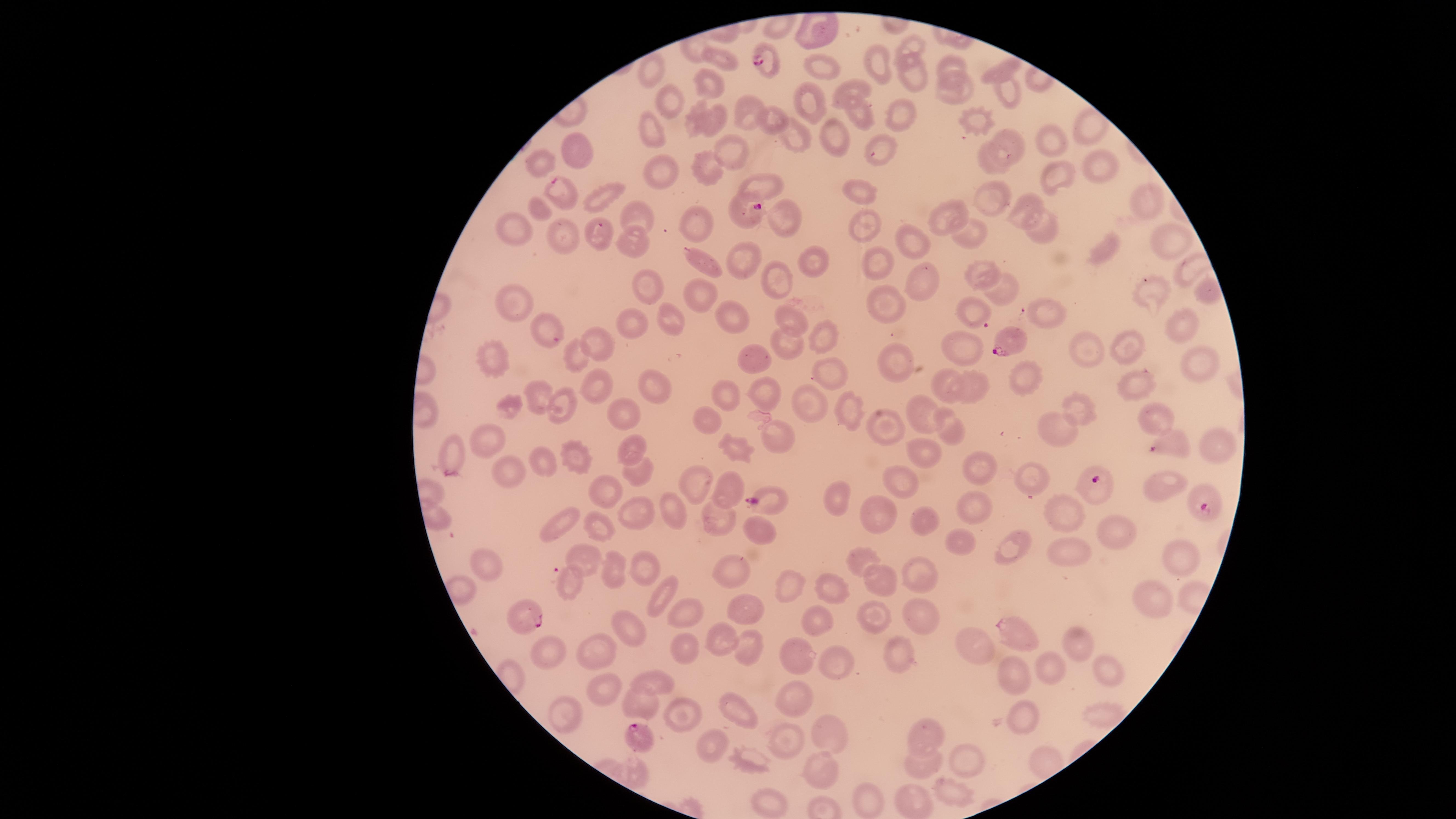
Approximate marker points as {x, y} in pixels.
Summary:
  - Parasitized RBCs: {763, 58}, {558, 190}, {748, 212}, {1008, 344}, {1163, 446}, {1096, 487}, {765, 499}, {1203, 506}, {530, 620}, {1016, 632}, {635, 736}
  - Uninfected RBCs: {912, 47}, {716, 58}, {876, 65}, {954, 66}, {818, 68}, {651, 71}, {1002, 72}, {908, 76}, {707, 83}, {951, 88}, {1004, 90}, {845, 93}, {668, 104}, {805, 107}, {903, 116}, {747, 117}, {689, 118}, {715, 118}, {771, 118}, {862, 118}, {977, 123}, {1085, 126}, {654, 134}, {833, 136}, {1014, 139}, {799, 140}, {1057, 140}, {577, 149}, {878, 151}, {730, 152}, {539, 159}, {996, 161}, {1101, 165}, {660, 171}, {711, 173}, {1047, 177}, {758, 188}, {602, 192}, {863, 193}, {991, 195}, {1139, 204}, {539, 206}, {1020, 207}, {632, 211}, {785, 219}, {952, 219}, {512, 222}, {701, 224}, {863, 227}, {1052, 228}, {598, 237}, {974, 237}, {910, 238}, {570, 241}, {1166, 241}, {633, 242}, {1103, 253}, {744, 257}, {706, 263}, {811, 263}, {987, 265}, {878, 266}, {919, 271}, {781, 280}, {999, 283}, {650, 287}, {708, 289}, {1153, 289}, {887, 296}, {512, 301}, {965, 310}, {1042, 312}, {731, 314}, {677, 317}, {788, 318}, {1185, 318}, {642, 329}, {548, 335}, {822, 341}, {786, 342}, {599, 343}, {1123, 343}, {968, 352}, {1092, 352}, {579, 358}, {902, 360}, {1205, 361}, {752, 363}, {494, 364}, {824, 368}, {1024, 379}, {944, 380}, {1137, 382}, {657, 385}, {979, 388}, {593, 389}, {762, 389}, {537, 394}, {728, 398}, {813, 400}, {1078, 406}, {568, 407}, {912, 407}, {848, 409}, {624, 415}, {1156, 415}, {703, 416}, {946, 418}, {885, 423}, {1051, 426}, {780, 432}, {485, 437}, {1220, 445}, {734, 447}, {634, 448}, {925, 450}, {456, 453}, {578, 453}, {542, 460}, {976, 467}, {509, 470}, {632, 472}, {1035, 477}, {904, 481}, {693, 483}, {1161, 483}, {728, 487}, {606, 489}, {838, 499}, {1058, 504}, {973, 506}, {673, 509}, {634, 514}, {875, 517}, {923, 517}, {715, 522}, {561, 523}, {601, 529}, {754, 530}, {1117, 531}, {958, 543}, {1068, 552}, {1182, 554}, {1017, 555}, {860, 557}, {490, 562}, {581, 562}, {910, 568}, {651, 570}, {737, 570}, {614, 571}, {879, 579}, {828, 584}, {565, 585}, {794, 586}, {662, 594}, {1150, 600}, {918, 606}, {747, 608}, {686, 615}, {819, 615}, {871, 616}, {629, 626}, {720, 642}, {1078, 644}, {970, 646}, {748, 648}, {551, 649}, {685, 650}, {893, 651}, {796, 653}, {597, 656}, {835, 661}, {1103, 666}, {1047, 668}, {1016, 677}, {653, 683}, {608, 687}, {796, 699}, {642, 702}, {1026, 711}, {567, 713}, {683, 713}, {744, 716}, {825, 735}, {787, 737}, {931, 737}, {712, 748}, {970, 758}, {747, 760}, {928, 767}, {633, 770}, {822, 773}, {958, 787}, {769, 801}, {869, 803}, {909, 803}
  - Preparation: thin blood smear
  - Species: Plasmodium falciparum
  - Capture: smartphone photograph through the microscope eyepiece
  - Visible region: circular
  - Presence: malaria parasites detected
  - Stain: Giemsa
  - Field of view: single
  - Image size: 1456×819 pixels